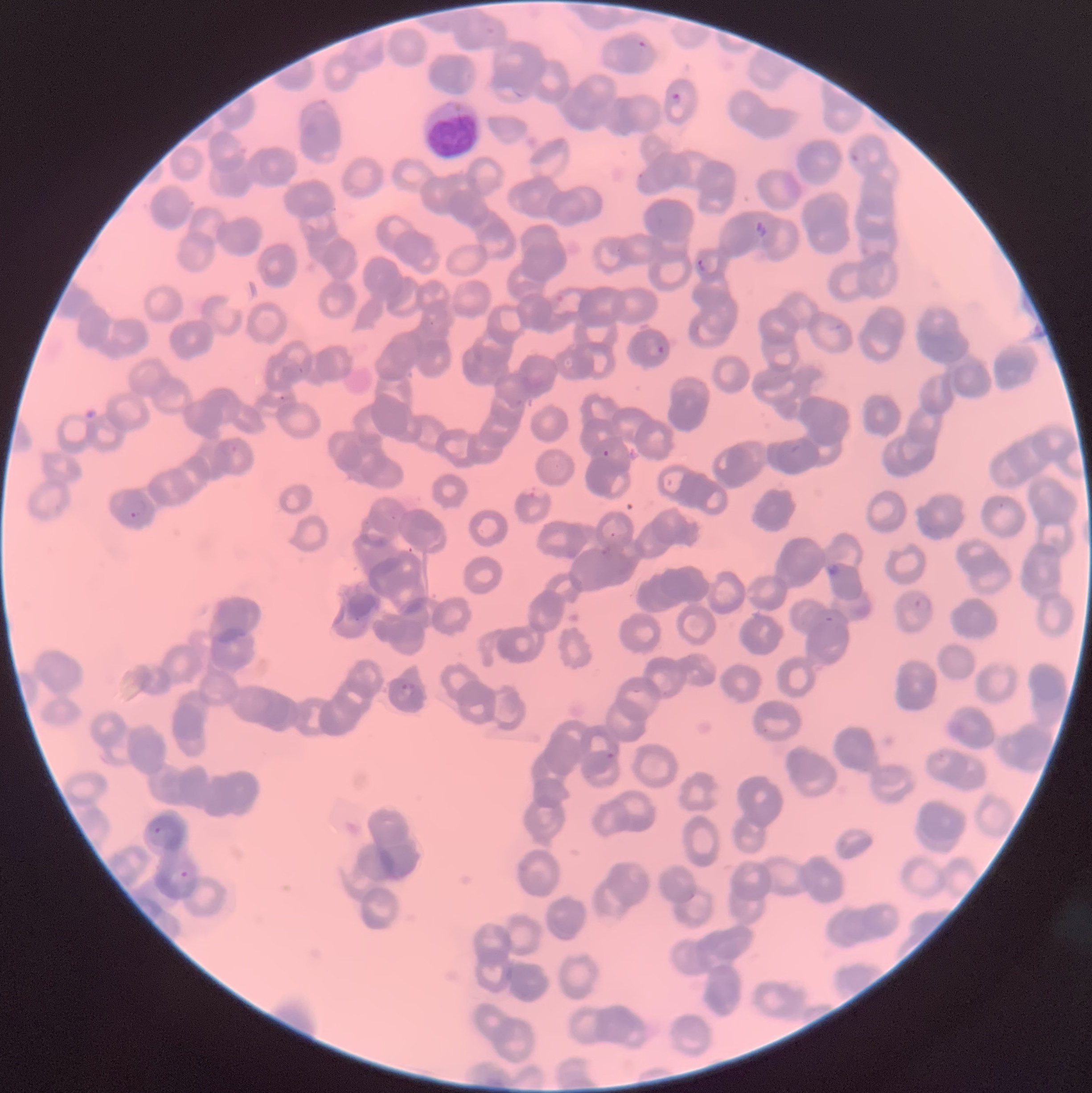

Summary:
  - Coordinate format: approximate bounding boxes as (x1, y1, x2, y2) in pixels
  - Plasmodium parasites too small for a box (approximate centers as (x, y) in pixels): (300, 369), (282, 397)
  - White blood cell locations: (420, 99, 484, 161)
  - Plasmodium parasite locations: (637, 40, 646, 48), (668, 92, 680, 104), (850, 150, 861, 163), (696, 257, 708, 274), (656, 345, 666, 355), (602, 449, 610, 457), (525, 487, 543, 498), (130, 497, 147, 520), (609, 531, 617, 539), (913, 595, 933, 614), (400, 681, 419, 696), (606, 741, 620, 760), (152, 826, 163, 835), (178, 870, 189, 879)
  - Preparation: thin blood film
  - Modality: light microscopy
  - Red blood cell morphology: rouleaux formation
  - Image size: 1092×1093 pixels